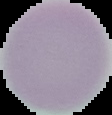

Malaria status: uninfected. Image is 112×115 pixels. Cell region segmented out of the field of view; the surrounding area is masked to black. From a thin blood smear.